Locate platelets.
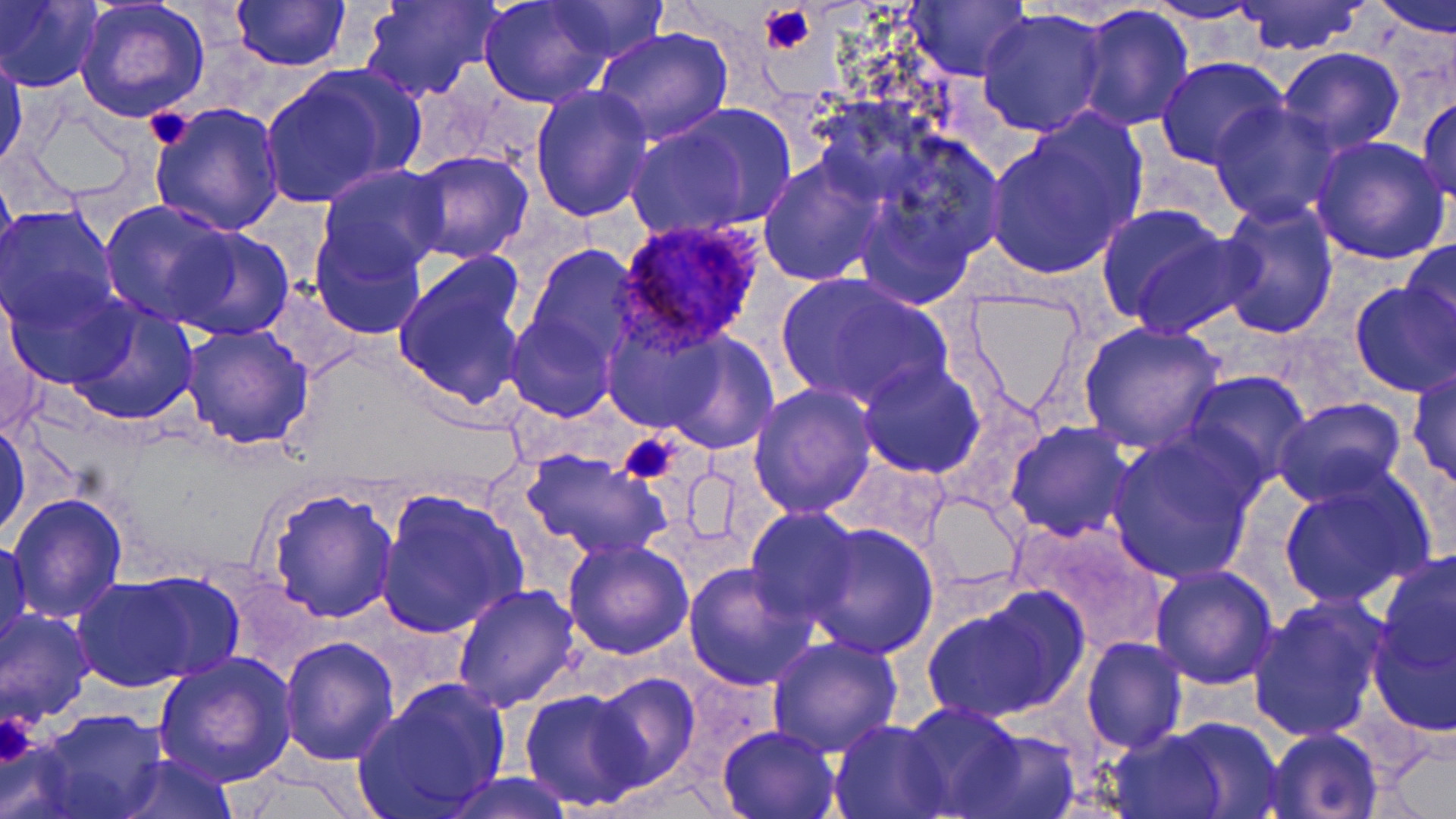

Approximate bounding boxes as (x1, y1, x2, y2) in pixels.
Platelets: (758, 2, 815, 55), (145, 107, 195, 152), (617, 433, 678, 485), (2, 710, 44, 767).

slide-level diagnosis = Plasmodium ovale
field of view = one of a larger specimen
modality = optical microscopy
magnification = 1000x
uninfected red blood cell locations = approximate bounding boxes as (x1, y1, x2, y2) in pixels: (358, 0, 500, 102), (479, 0, 614, 108), (1369, 0, 1456, 39), (0, 1, 102, 91), (75, 1, 210, 122), (229, 1, 349, 71), (545, 1, 668, 64), (903, 2, 1032, 82), (1143, 2, 1268, 25), (1234, 2, 1366, 56), (1075, 6, 1195, 133), (977, 8, 1111, 138), (593, 27, 736, 147), (1275, 48, 1406, 156), (1, 49, 25, 171), (1156, 56, 1288, 169), (264, 68, 410, 203), (530, 84, 653, 221), (1417, 96, 1456, 201), (149, 101, 286, 235), (1207, 101, 1344, 225), (626, 105, 794, 238), (1249, 117, 1407, 255), (984, 119, 1146, 280), (845, 135, 1002, 308), (1310, 135, 1452, 265), (403, 149, 535, 264), (758, 153, 885, 283), (317, 164, 446, 280), (0, 166, 20, 297), (1214, 198, 1341, 338), (100, 200, 236, 328), (1095, 203, 1246, 334), (1, 204, 120, 330), (311, 224, 425, 339), (166, 226, 293, 342), (1401, 238, 1456, 354), (523, 245, 644, 364), (392, 255, 528, 412), (775, 270, 950, 411), (1350, 280, 1456, 397), (4, 285, 130, 392), (963, 288, 1087, 419), (64, 299, 200, 427), (505, 312, 617, 422), (615, 317, 782, 449), (1077, 321, 1224, 453), (181, 322, 313, 450), (857, 360, 986, 479), (1406, 368, 1456, 487), (1183, 371, 1311, 490), (749, 384, 878, 520), (1272, 397, 1407, 507), (0, 414, 30, 542), (1004, 420, 1135, 541), (1105, 430, 1261, 585), (522, 450, 668, 561), (838, 457, 950, 554), (1277, 475, 1432, 608), (264, 487, 399, 623), (375, 489, 530, 639), (923, 491, 1025, 594), (7, 493, 128, 625), (746, 507, 860, 625), (1013, 519, 1171, 657), (804, 522, 941, 659), (1, 535, 30, 661), (562, 539, 695, 660), (1374, 547, 1455, 716), (682, 562, 818, 691), (1148, 563, 1279, 687), (124, 571, 245, 681), (72, 576, 204, 691), (452, 584, 582, 715), (922, 593, 1080, 725), (1247, 594, 1391, 744), (1, 610, 94, 729), (766, 635, 901, 758), (279, 636, 399, 764), (1081, 636, 1187, 753), (153, 651, 298, 791), (586, 672, 701, 791), (355, 679, 511, 818), (519, 688, 650, 810), (899, 705, 1029, 816), (30, 708, 170, 819), (1165, 715, 1284, 817), (829, 718, 949, 818), (717, 723, 840, 818), (1101, 727, 1239, 819), (1263, 727, 1385, 818), (953, 729, 1082, 819), (109, 754, 240, 818), (437, 773, 580, 819)
Plasmodium ovale-infected red blood cell locations = approximate bounding boxes as (x1, y1, x2, y2) in pixels: (614, 216, 767, 354)
image size = 1456×819 pixels
preparation = thin blood film
stain = May-Grünwald-Giemsa